Comment on the morphology of the red blood cells.
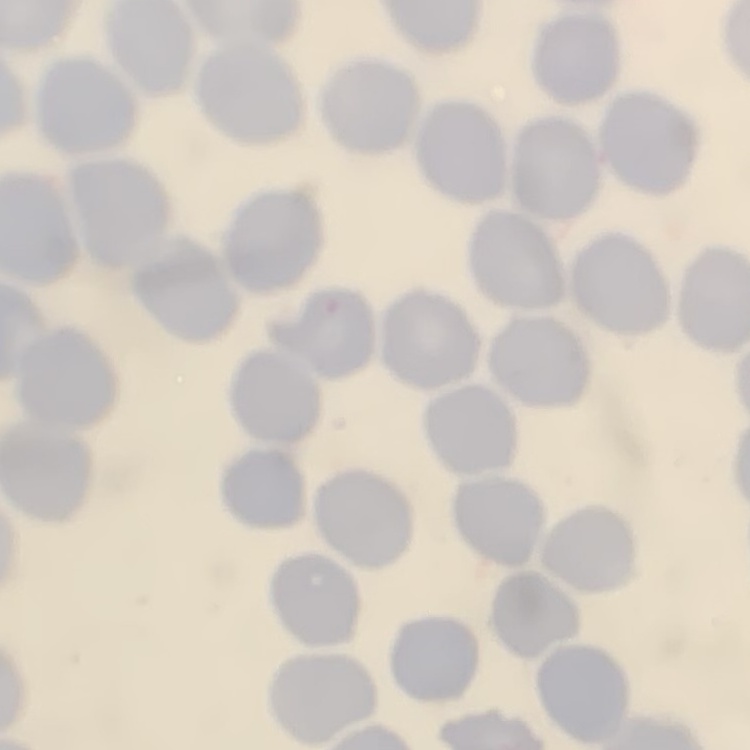

No rouleaux formation.

stain = Field's or Giemsa
preparation = thin peripheral smear
image type = square crop of a larger photomicrograph